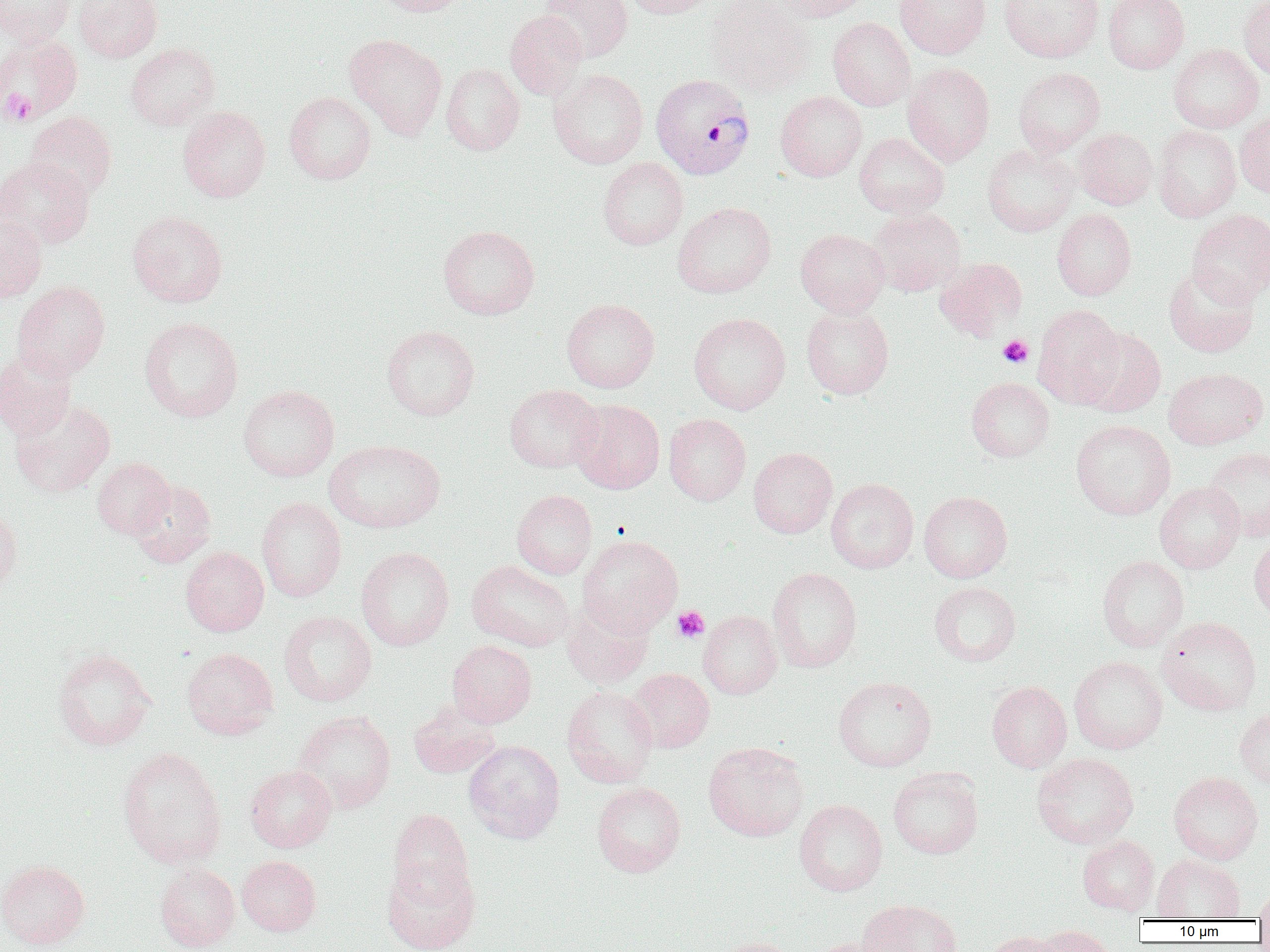
Summary:
  - Coordinate format: approximate bounding boxes as [x1, y1, x2, y2] in pixels
  - Uninfected red blood cell locations: [0, 0, 76, 45], [73, 0, 163, 62], [371, 0, 469, 16], [539, 0, 633, 62], [622, 0, 716, 19], [771, 0, 870, 21], [894, 0, 991, 59], [998, 0, 1105, 63], [1104, 0, 1190, 73], [1239, 0, 1270, 79], [705, 1, 816, 97], [504, 10, 589, 101], [828, 17, 916, 111], [344, 33, 447, 140], [0, 34, 83, 124], [125, 42, 220, 131], [1168, 44, 1264, 132], [902, 62, 995, 165], [441, 63, 524, 155], [1012, 67, 1106, 157], [549, 69, 648, 169], [284, 91, 376, 184], [775, 91, 867, 181], [178, 106, 271, 202], [25, 112, 117, 201], [1235, 112, 1270, 198], [1152, 125, 1241, 222], [1074, 128, 1157, 209], [854, 132, 949, 218], [982, 144, 1079, 236], [0, 157, 94, 249], [598, 157, 688, 250], [673, 202, 776, 298], [869, 208, 967, 296], [1052, 208, 1136, 300], [1187, 209, 1270, 305], [127, 210, 228, 307], [0, 212, 47, 302], [437, 225, 540, 320], [795, 228, 890, 316], [934, 257, 1028, 341], [1163, 265, 1260, 357], [11, 281, 110, 381], [562, 299, 660, 393], [801, 304, 894, 399], [1032, 304, 1125, 408], [688, 312, 791, 414], [139, 317, 243, 422], [381, 325, 480, 420], [1077, 327, 1166, 417], [0, 349, 77, 440], [1164, 367, 1268, 450], [966, 377, 1055, 462], [504, 384, 603, 473], [238, 385, 339, 481], [10, 399, 115, 498], [570, 399, 665, 494], [664, 413, 751, 505], [1071, 419, 1176, 520], [324, 439, 445, 533], [748, 447, 838, 538], [1204, 447, 1270, 541], [92, 458, 174, 539], [825, 478, 919, 573], [129, 479, 216, 568], [1155, 481, 1245, 573], [512, 489, 597, 579], [919, 491, 1012, 582], [257, 497, 346, 601], [0, 507, 22, 596], [578, 534, 683, 636], [1249, 534, 1270, 621], [181, 546, 269, 636], [356, 547, 455, 651], [1097, 555, 1189, 651], [467, 560, 574, 651], [767, 567, 862, 672], [929, 581, 1021, 667], [561, 600, 653, 689], [278, 610, 376, 706], [698, 610, 783, 699], [1156, 616, 1262, 716], [447, 641, 537, 728], [182, 647, 278, 739], [52, 648, 156, 751], [1069, 656, 1167, 754], [628, 668, 714, 753], [833, 676, 937, 771], [987, 681, 1072, 773], [561, 685, 658, 787], [408, 703, 502, 779], [1235, 706, 1270, 788], [293, 711, 396, 813], [463, 740, 565, 843], [703, 742, 809, 841], [117, 747, 227, 868], [1032, 752, 1139, 848], [245, 765, 336, 853], [888, 767, 983, 859], [1168, 771, 1264, 864], [592, 782, 686, 877], [794, 799, 887, 896], [388, 809, 474, 905], [1077, 835, 1159, 915], [1152, 854, 1245, 920], [236, 855, 321, 936], [0, 860, 90, 950], [382, 860, 480, 952], [154, 862, 240, 951], [1254, 886, 1270, 923], [856, 899, 962, 952], [1035, 925, 1116, 952], [981, 930, 1066, 952], [709, 936, 802, 952], [807, 937, 895, 952]
  - Plasmodium vivax-infected red blood cell locations: [651, 72, 756, 180]
  - Platelet locations: [0, 89, 37, 126], [998, 334, 1033, 368], [672, 606, 709, 642]
  - Slide-level diagnosis: Plasmodium vivax
  - Preparation: thin blood smear
  - Modality: light microscopy
  - Magnification: 1000x
  - Field of view: one of a larger specimen
  - Image size: 1270×952 pixels